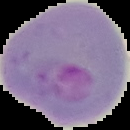

Summary:
  - Malaria status: parasitized
  - Preparation: thin blood film
  - Image type: segmented cell region on a black background
  - Image size: 130×130 pixels